Report the malaria status of this cell.
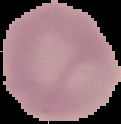
Uninfected.

Summary:
  - Image type: segmented cell region with the area outside set to black
  - Image size: 121×124 pixels
  - Preparation: thin blood film